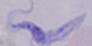

magnification = 1000x
identification = trypanosome
modality = photomicrograph